State the blood parasite species.
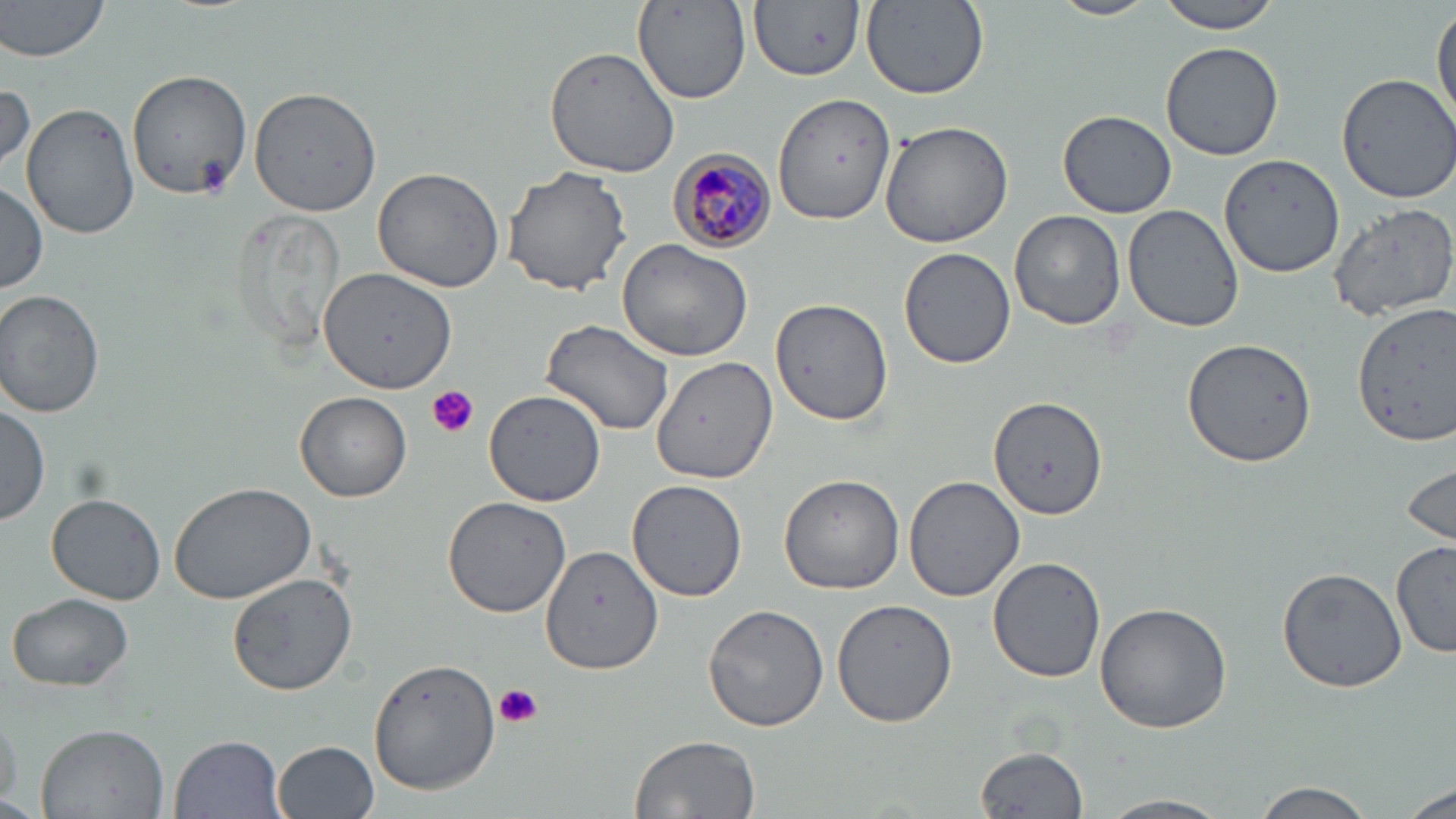
Plasmodium malariae.

Approximate bounding boxes as named x1/y1/x2/y2 corners in pixels. Platelet locations: (x1=193, y1=156, x2=234, y2=196), (x1=426, y1=386, x2=479, y2=439), (x1=494, y1=682, x2=543, y2=728). Uninfected red blood cell locations: (x1=0, y1=0, x2=111, y2=61), (x1=750, y1=0, x2=865, y2=81), (x1=861, y1=0, x2=990, y2=100), (x1=1052, y1=0, x2=1157, y2=22), (x1=1157, y1=0, x2=1284, y2=33), (x1=632, y1=1, x2=749, y2=106), (x1=1432, y1=2, x2=1456, y2=126), (x1=1160, y1=41, x2=1284, y2=161), (x1=543, y1=45, x2=683, y2=179), (x1=127, y1=66, x2=250, y2=197), (x1=1333, y1=74, x2=1456, y2=205), (x1=0, y1=82, x2=34, y2=177), (x1=248, y1=87, x2=383, y2=216), (x1=772, y1=92, x2=895, y2=226), (x1=21, y1=101, x2=141, y2=238), (x1=1059, y1=109, x2=1176, y2=217), (x1=875, y1=118, x2=1015, y2=249), (x1=1218, y1=152, x2=1346, y2=281), (x1=502, y1=166, x2=632, y2=296), (x1=372, y1=167, x2=506, y2=293), (x1=0, y1=182, x2=48, y2=296), (x1=1327, y1=201, x2=1456, y2=320), (x1=1121, y1=204, x2=1243, y2=333), (x1=227, y1=207, x2=349, y2=356), (x1=1009, y1=211, x2=1125, y2=331), (x1=616, y1=238, x2=754, y2=361), (x1=898, y1=247, x2=1017, y2=370), (x1=310, y1=266, x2=457, y2=397), (x1=0, y1=289, x2=106, y2=418), (x1=769, y1=297, x2=894, y2=427), (x1=1352, y1=302, x2=1455, y2=443), (x1=541, y1=320, x2=676, y2=437), (x1=1182, y1=337, x2=1316, y2=467), (x1=652, y1=355, x2=779, y2=484), (x1=483, y1=389, x2=607, y2=506), (x1=295, y1=392, x2=413, y2=502), (x1=988, y1=395, x2=1107, y2=519), (x1=0, y1=402, x2=50, y2=525), (x1=1400, y1=456, x2=1455, y2=551), (x1=778, y1=473, x2=905, y2=594), (x1=903, y1=475, x2=1025, y2=603), (x1=168, y1=479, x2=319, y2=604), (x1=626, y1=480, x2=748, y2=603), (x1=46, y1=494, x2=166, y2=605), (x1=441, y1=495, x2=572, y2=618), (x1=1393, y1=538, x2=1455, y2=660), (x1=543, y1=545, x2=663, y2=673), (x1=987, y1=556, x2=1106, y2=683), (x1=1276, y1=565, x2=1407, y2=693), (x1=226, y1=573, x2=360, y2=697), (x1=7, y1=591, x2=135, y2=692), (x1=832, y1=598, x2=959, y2=726), (x1=703, y1=602, x2=831, y2=731), (x1=1093, y1=602, x2=1233, y2=735), (x1=368, y1=656, x2=499, y2=797), (x1=0, y1=698, x2=23, y2=810), (x1=37, y1=723, x2=169, y2=819), (x1=169, y1=733, x2=286, y2=818), (x1=628, y1=734, x2=761, y2=819), (x1=274, y1=739, x2=381, y2=819), (x1=974, y1=740, x2=1091, y2=817), (x1=1249, y1=780, x2=1378, y2=818), (x1=1393, y1=785, x2=1455, y2=818), (x1=1098, y1=793, x2=1233, y2=818). Plasmodium malariae-infected red blood cell locations: (x1=667, y1=151, x2=775, y2=252). May-Grünwald-Giemsa stain. Optical microscopy. Thin blood film. Single field of view. Image is 1456×819 pixels. Captured at 1000x magnification.